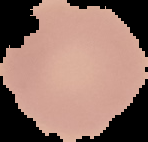

image size = 148×142 pixels
image type = segmented cell region on a black background
result = no Plasmodium parasites detected
preparation = thin blood film